Assess the morphology of the red blood cells.
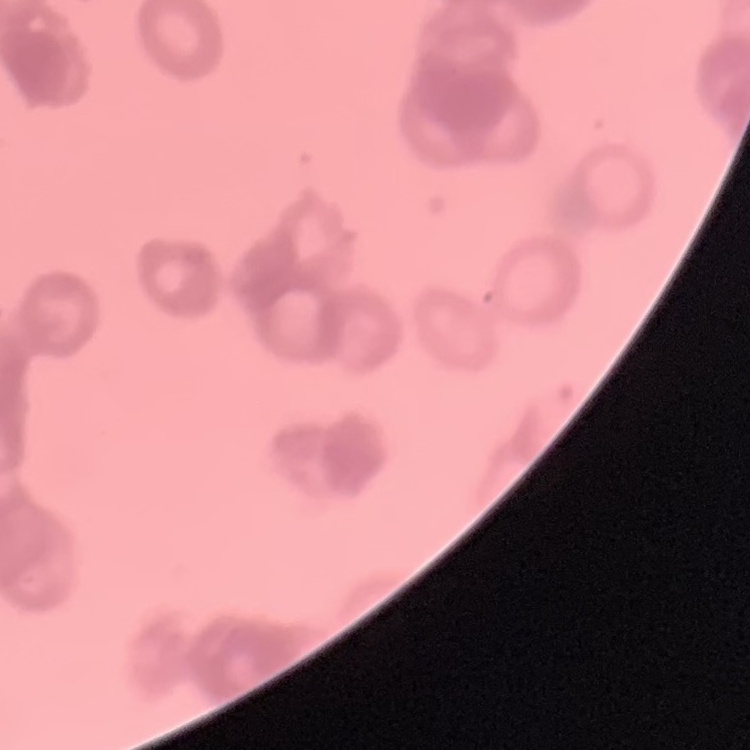
Rouleaux formation.

Thin blood smear. Square crop of a larger photomicrograph. Stained with either Field's or Giemsa.